State which parasite is depicted.
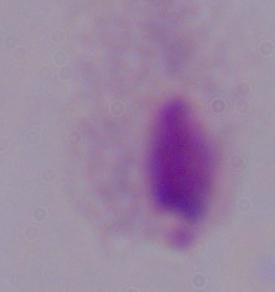
A trichomonad.

Summary:
  - Magnification: 1000x
  - Modality: photomicrograph